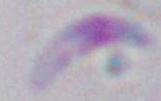

identification = Toxoplasma gondii
modality = photomicrograph
magnification = 1000x